Locate and identify every blood parasite.
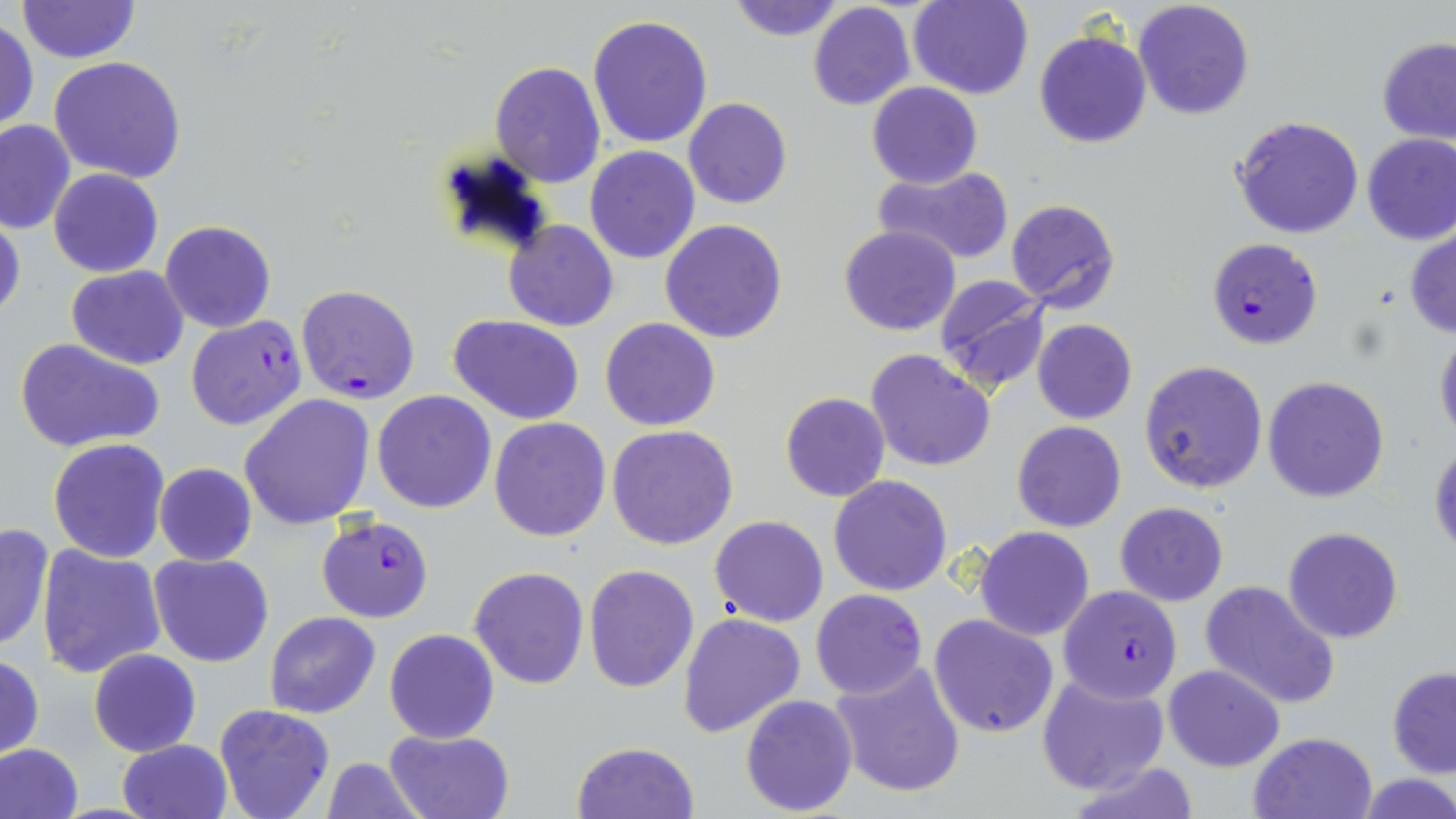
Approximate bounding boxes as (x1, y1, x2, y2) in pixels.
Plasmodium falciparum-infected red blood cells: (1207, 238, 1322, 350), (295, 283, 421, 405), (184, 315, 307, 431), (314, 512, 434, 623), (1057, 584, 1183, 704), (810, 589, 929, 698).
No Plasmodium ovale, Plasmodium malariae, Plasmodium vivax, Babesia divergens, or Trypanosoma brucei observed.

slide_level_diagnosis: Plasmodium falciparum
preparation: thin blood film
uninfected_red_blood_cell_locations: 'approximate bounding boxes as (x1, y1, x2, y2) in pixels: (15, 0, 140, 65), (724, 0, 846, 41), (908, 0, 1033, 100), (1134, 0, 1254, 120), (807, 3, 916, 112), (587, 14, 713, 149), (1, 19, 39, 133), (1034, 29, 1152, 149), (1377, 37, 1456, 144), (47, 56, 189, 184), (490, 60, 605, 188), (866, 82, 982, 188), (683, 98, 792, 209), (1227, 115, 1366, 240), (0, 119, 75, 234), (1362, 133, 1456, 245), (585, 146, 701, 264), (871, 166, 1017, 268), (48, 168, 163, 277), (1005, 198, 1122, 313), (0, 209, 23, 327), (502, 219, 617, 331), (660, 219, 788, 342), (159, 220, 276, 334), (839, 224, 961, 336), (1405, 227, 1456, 338), (67, 265, 189, 370), (933, 274, 1052, 394), (449, 315, 587, 422), (601, 318, 720, 432), (1032, 319, 1137, 424), (1434, 327, 1456, 444), (16, 338, 164, 455), (864, 349, 996, 471), (1139, 360, 1269, 494), (1262, 376, 1390, 503), (371, 391, 497, 513), (780, 393, 890, 503), (238, 394, 376, 530), (488, 416, 612, 542), (1012, 421, 1126, 532), (607, 424, 740, 550), (1429, 437, 1456, 555), (49, 438, 170, 562), (154, 463, 258, 566), (828, 474, 953, 596), (1114, 502, 1228, 606), (710, 516, 828, 626), (0, 522, 54, 655), (974, 527, 1094, 641), (1283, 527, 1402, 644), (36, 546, 167, 680), (149, 553, 274, 668), (583, 563, 700, 693), (469, 566, 590, 689), (1199, 581, 1341, 709), (265, 612, 380, 718), (678, 613, 804, 739), (928, 613, 1059, 738), (384, 629, 498, 744), (87, 649, 201, 757), (0, 653, 44, 759), (829, 659, 968, 798), (1163, 664, 1284, 771), (1386, 667, 1456, 778), (1037, 676, 1168, 793), (740, 694, 858, 816), (214, 704, 337, 819), (383, 727, 513, 819), (1249, 730, 1378, 819), (119, 738, 231, 818), (571, 742, 700, 819), (0, 743, 83, 819), (320, 757, 428, 817), (1067, 762, 1204, 819), (1360, 775, 1456, 818)'
field_of_view: one of a larger specimen
magnification: 1000x
modality: light microscopy
stain: May-Grünwald-Giemsa
image_size: 1456×819 pixels